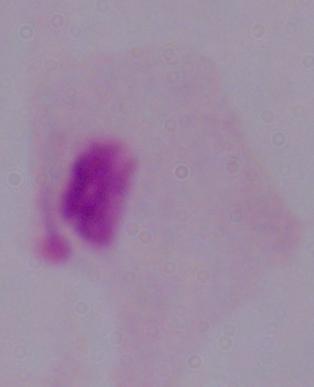

Summary:
  - Modality: photomicrograph
  - Magnification: 1000x
  - Identification: trichomonad